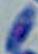

Summary:
  - Modality: photomicrograph
  - Magnification: 1000x
  - Identification: Toxoplasma gondii